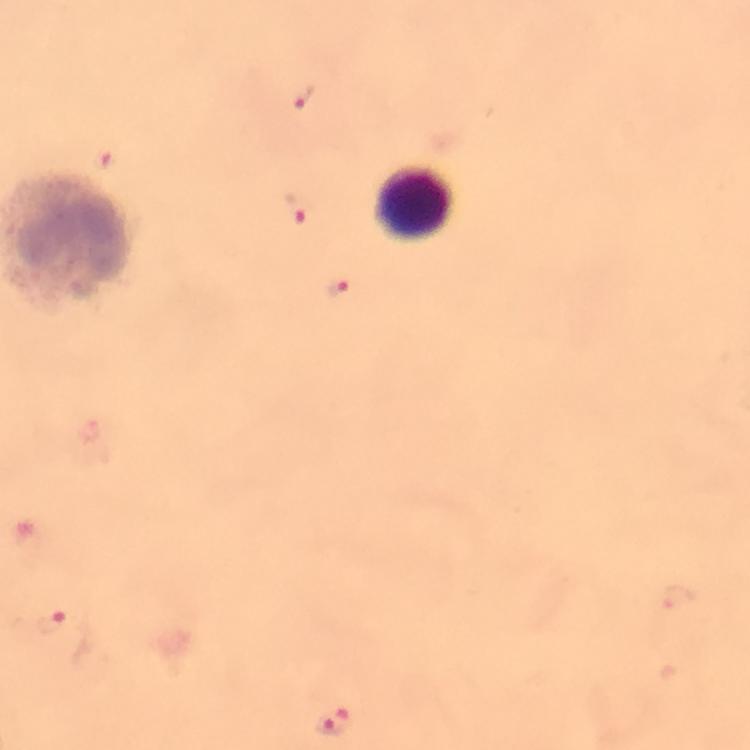

Approximate centers as {x, y} in pixels.
Summary:
  - Leukocyte locations: {414, 205}
  - Malaria parasite locations: {303, 96}, {105, 159}, {297, 207}, {336, 287}, {51, 621}, {334, 720}
  - Image size: 750×750 pixels
  - Preparation: thick smear
  - Immersion oil: used
  - Cropped from: one field of view
  - Capture: smartphone camera through the microscope
  - Magnification: 100x
  - Context: from a malaria diagnostic workup
  - Stain: Giemsa